Report the malaria status of this cell.
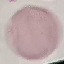

Uninfected.

Cell patch, automatically extracted from a larger field of view and resized to 64 × 64 pixels. Photographed with a smartphone camera at the microscope eyepiece. Thin smear of blood. Giemsa-stained preparation.